Name the blood parasite species.
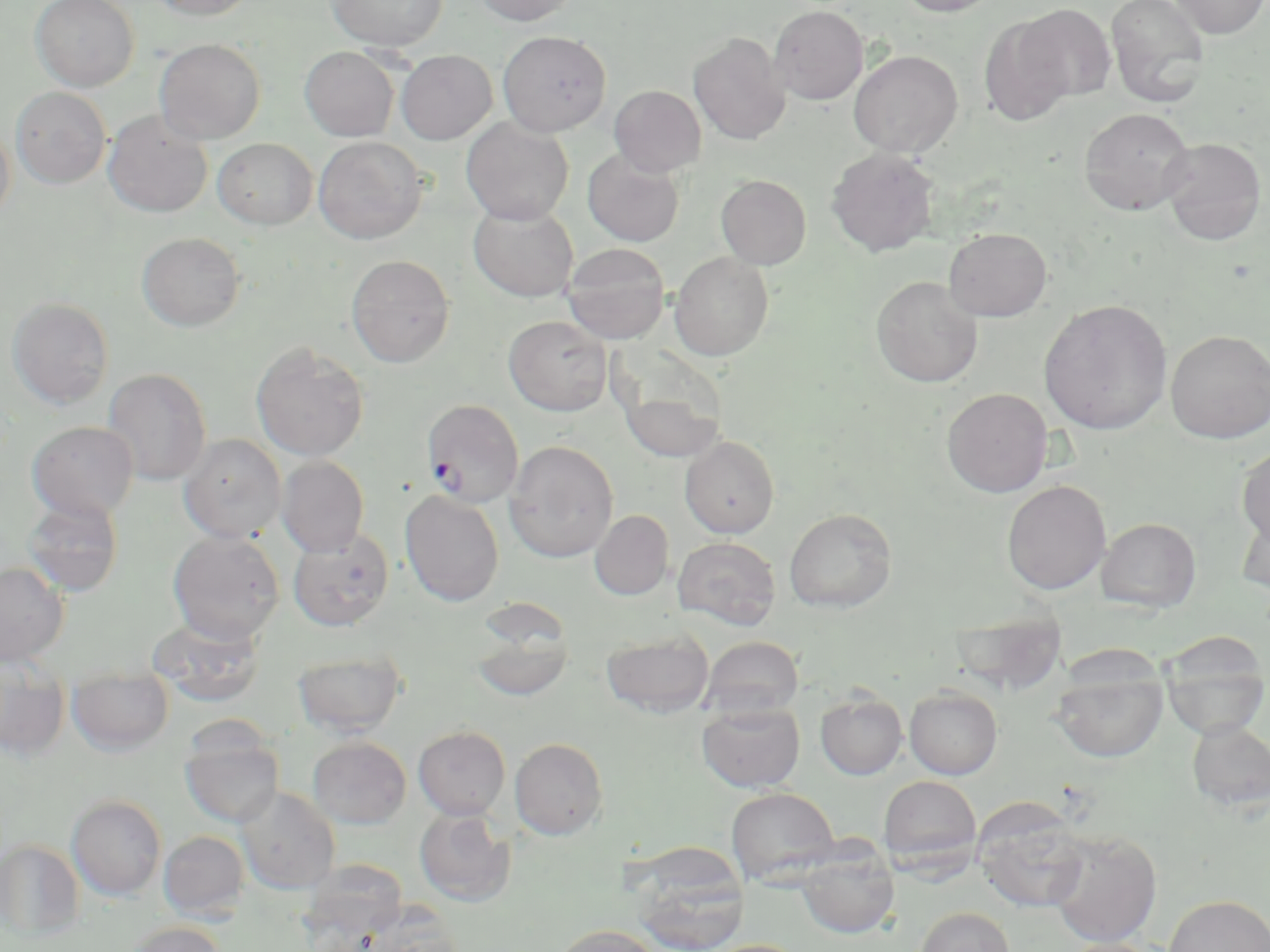

Plasmodium falciparum.

Approximate bounding boxes as (x1, y1, x2, y2) in pixels. Uninfected red blood cell locations: (30, 0, 139, 91), (148, 0, 256, 20), (327, 0, 447, 51), (473, 0, 579, 25), (895, 0, 1002, 16), (1105, 0, 1210, 109), (1170, 0, 1269, 38), (1016, 4, 1115, 102), (769, 5, 869, 105), (978, 16, 1075, 126), (497, 30, 611, 136), (689, 33, 791, 145), (154, 38, 265, 144), (299, 46, 399, 141), (848, 49, 963, 157), (395, 50, 497, 145), (609, 85, 706, 176), (11, 87, 111, 189), (1079, 107, 1195, 215), (103, 111, 213, 217), (461, 117, 574, 225), (0, 121, 15, 229), (313, 136, 427, 244), (1159, 137, 1267, 245), (213, 138, 318, 230), (826, 147, 940, 258), (582, 149, 685, 247), (716, 174, 811, 269), (468, 202, 579, 302), (943, 227, 1052, 321), (137, 231, 245, 332), (562, 243, 670, 343), (669, 251, 774, 360), (346, 254, 455, 367), (871, 275, 984, 388), (6, 297, 114, 409), (1039, 298, 1172, 435), (503, 315, 612, 416), (1165, 329, 1270, 443), (250, 342, 369, 462), (102, 368, 211, 486), (614, 369, 727, 465), (941, 388, 1053, 497), (27, 421, 138, 521), (179, 434, 286, 543), (679, 435, 780, 538), (504, 440, 619, 563), (1236, 446, 1270, 551), (277, 456, 369, 557), (1002, 480, 1111, 595), (400, 489, 504, 606), (22, 495, 124, 597), (784, 507, 897, 612), (1236, 507, 1270, 598), (590, 510, 674, 600), (1096, 517, 1201, 612), (288, 529, 393, 631), (167, 531, 285, 644), (673, 537, 780, 630), (0, 561, 69, 666), (952, 611, 1068, 696), (147, 615, 267, 708), (469, 617, 575, 701), (601, 631, 714, 718), (1158, 632, 1270, 738), (702, 636, 804, 719), (293, 649, 407, 738), (1051, 665, 1167, 763), (67, 668, 174, 756), (0, 675, 70, 759), (904, 686, 1003, 779), (815, 691, 907, 779), (697, 701, 805, 792), (1186, 719, 1270, 812), (413, 725, 511, 819), (179, 731, 284, 828), (307, 736, 412, 829), (510, 738, 608, 840), (878, 775, 981, 871), (237, 787, 340, 895), (726, 787, 840, 884), (66, 795, 167, 900), (973, 800, 1090, 914), (414, 807, 516, 907), (1046, 829, 1162, 947), (158, 830, 250, 921), (0, 840, 85, 939), (796, 844, 898, 938), (632, 860, 747, 952), (1163, 894, 1270, 952), (364, 905, 465, 952), (915, 906, 1014, 952), (126, 921, 226, 952), (551, 924, 662, 952), (1056, 938, 1165, 952), (704, 939, 810, 952). Plasmodium falciparum-infected red blood cell locations: (420, 399, 524, 508). Captured at 1000x magnification. Image is 1270×952 pixels. Thin blood smear. May-Grünwald-Giemsa-stained preparation. Optical microscopy. Single field of view.